Report the malaria status of this cell.
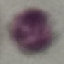
It is uninfected.

image type = automatically extracted cell patch, resized to 64 × 64 pixels
preparation = thin blood smear
capture = smartphone camera at the microscope eyepiece
stain = Giemsa